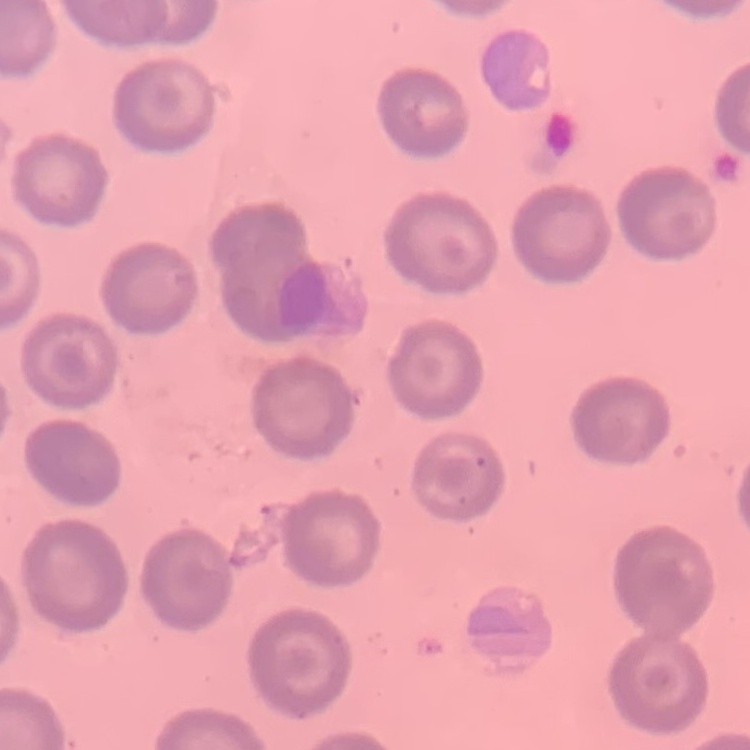

Summary:
  - Red blood cell morphology: no rouleaux formation
  - Preparation: thin blood film
  - Image type: one tile cut from a larger photomicrograph
  - Stain: Field's or Giemsa